Classify this cell by malaria status.
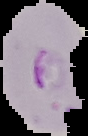
Parasitized.

Summary:
  - Preparation: thin blood smear
  - Image type: segmented cell region on a black background
  - Image size: 88×136 pixels